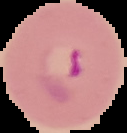

From a thin blood smear. Image is 127×133 pixels. Result: malaria parasites identified. Segmented cell region on a black background.